Report the malaria status of this cell.
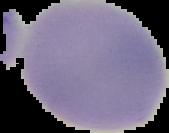
Uninfected.

Summary:
  - Image size: 169×133 pixels
  - Preparation: thin blood smear
  - Image type: segmented cell region on a black background